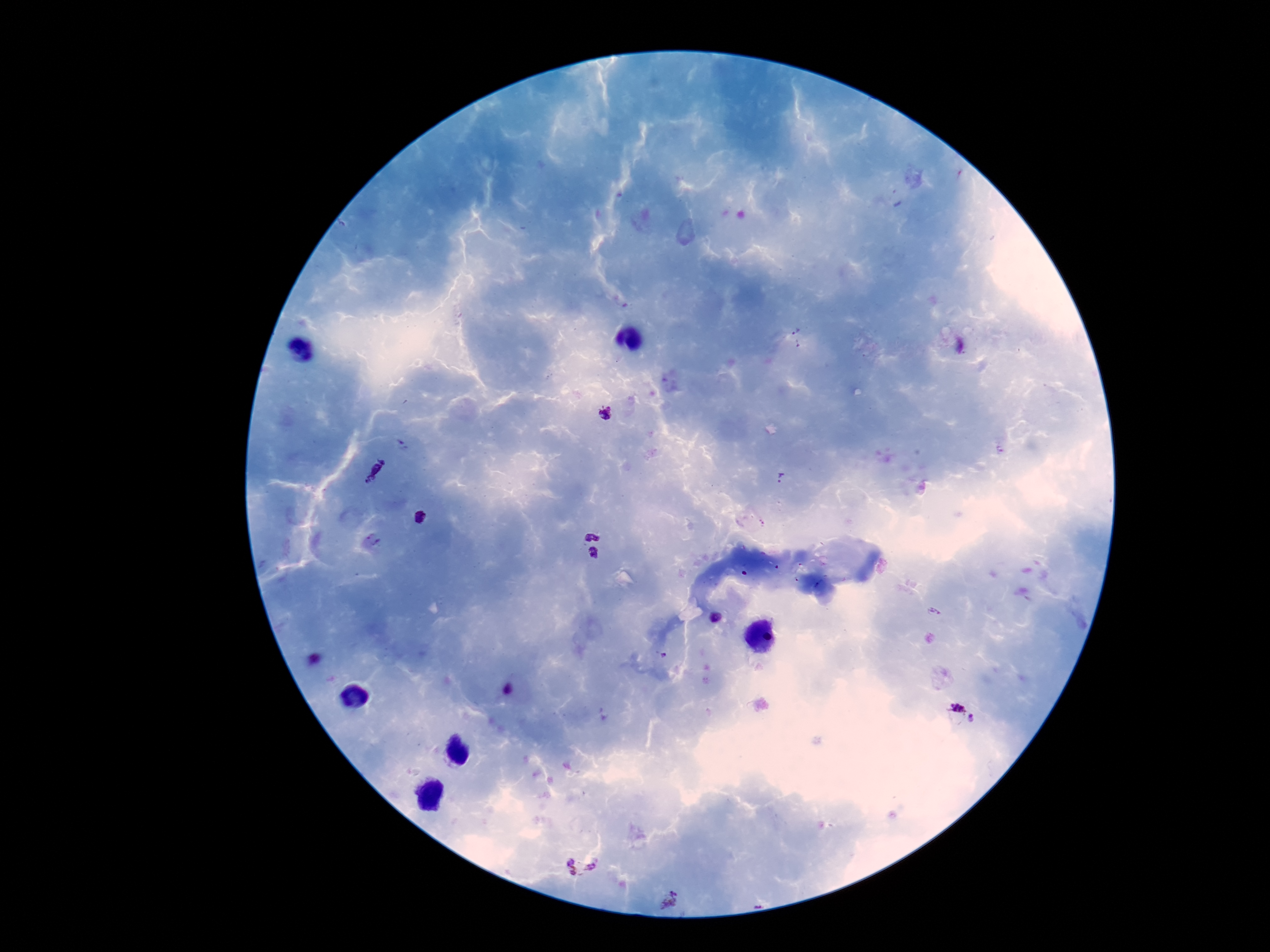

Approximate object centers, in pixels from the top-left corner.
Summary:
  - Plasmodium parasite locations: (x=797, y=337), (x=606, y=414), (x=375, y=469), (x=782, y=479), (x=420, y=518), (x=591, y=535), (x=374, y=539), (x=595, y=553), (x=934, y=611), (x=714, y=617), (x=663, y=656), (x=316, y=660), (x=509, y=690), (x=956, y=711), (x=973, y=719), (x=582, y=864), (x=670, y=900)
  - Patient malaria status: infected
  - Field of view: one from this slide
  - Image size: 1270×952 pixels
  - Preparation: thick blood film
  - Magnification: 100x
  - Stain: Giemsa
  - Capture: smartphone camera through the microscope eyepiece